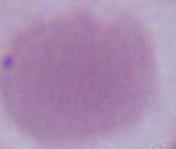
magnification: 1000x
identification: red blood cell
modality: photomicrograph